Give the extent of the malaria parasites you find, grouped by life-cycle stage — ring form, trophozoite, schizont, or gametocyte.
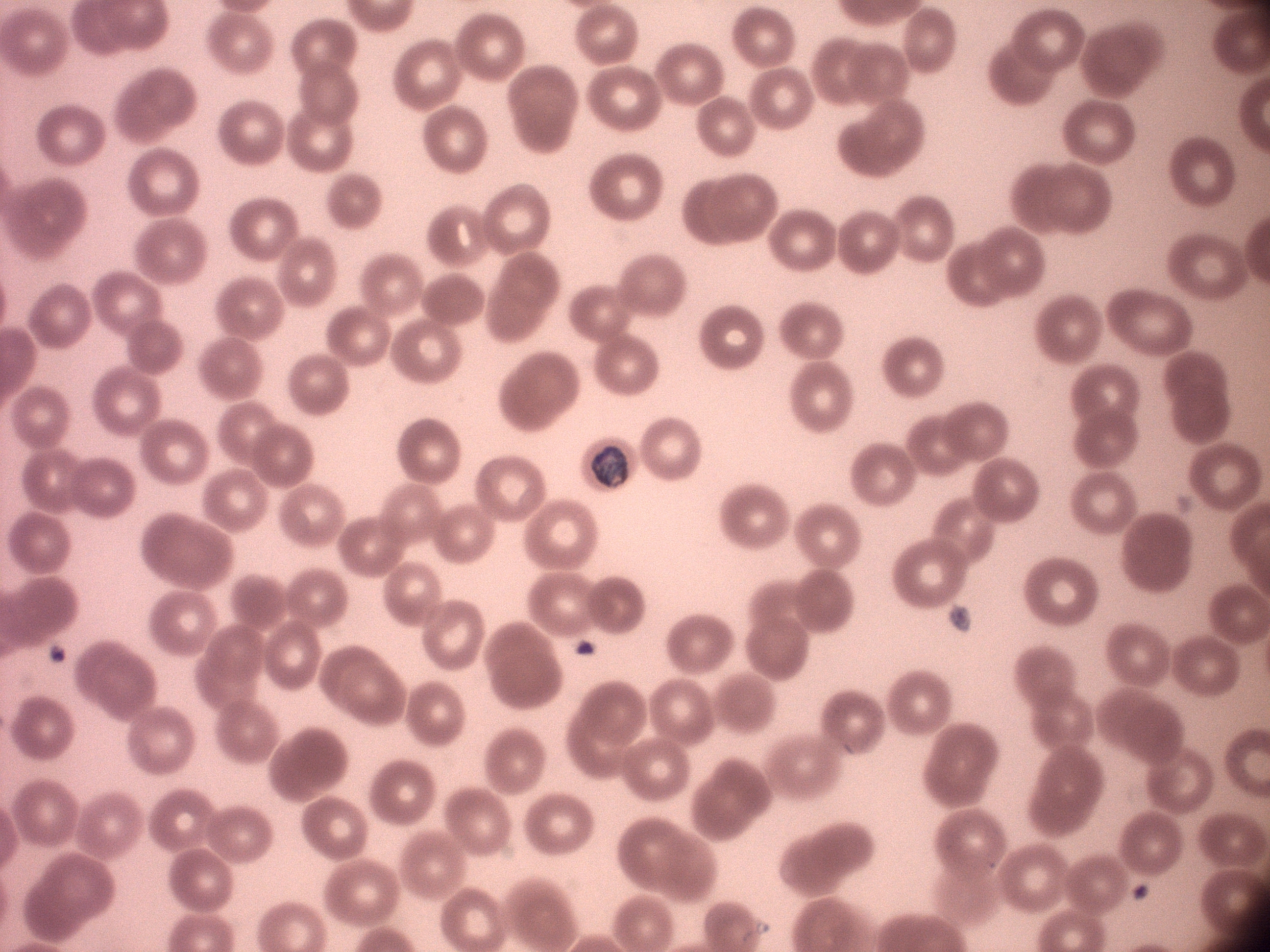
Approximate bounding boxes as [x1, y1, x2, y2] in pixels, from the source annotation, which is not necessarily exhaustive.
Trophozoites: [591, 446, 630, 487].

Summary:
  - Microscope: Leica DM2000 with built-in camera
  - Field of view: one from this slide
  - Stain: Giemsa
  - Magnification: 100x
  - Species: Plasmodium malariae
  - Preparation: thin blood film
  - Image size: 1270×952 pixels